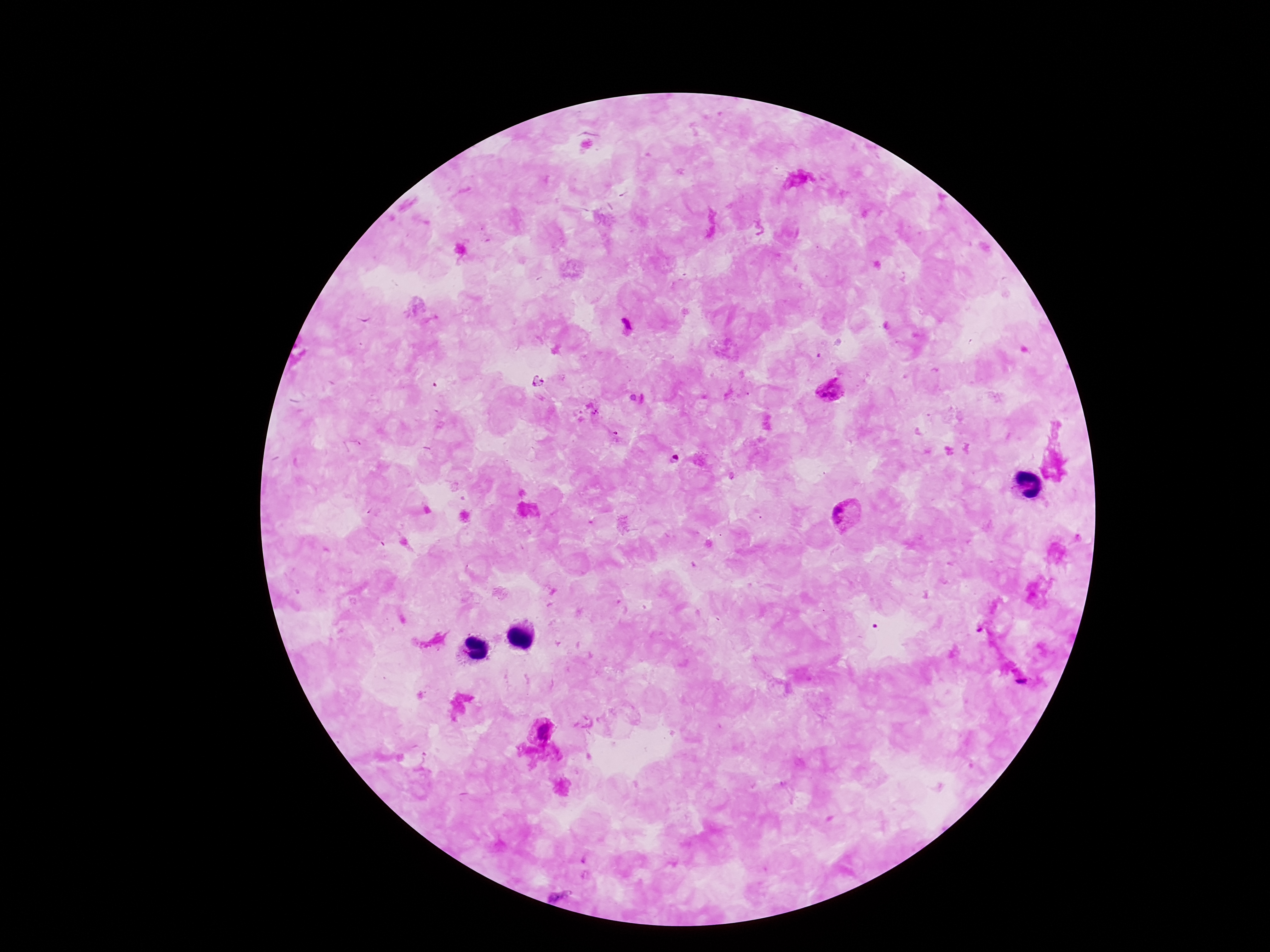 Approximate centers as [x, y] in pixels. Plasmodium parasite locations: [627, 326], [830, 390], [848, 518], [541, 729]. Giemsa-stained preparation. Single field of view. Patient malaria status: positive. Thick peripheral-blood smear. 100x magnification. Smartphone photograph taken through the microscope eyepiece. Image is 1270×952 pixels.